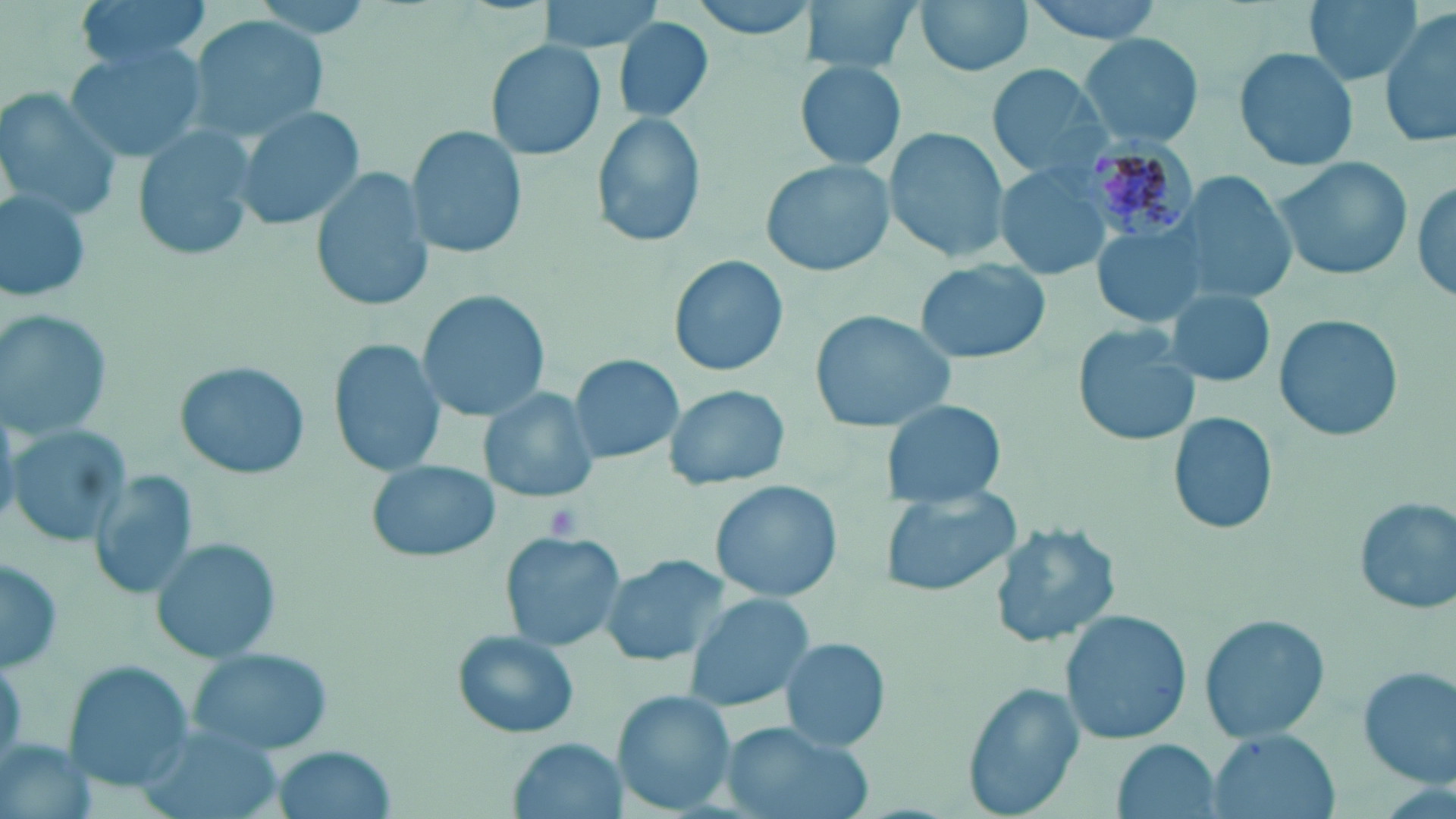 Approximate bounding boxes as [x1, y1, x2, y2] in pixels. Uninfected red blood cell locations: [73, 0, 216, 67], [533, 0, 667, 52], [683, 0, 818, 40], [806, 0, 920, 71], [913, 0, 1035, 78], [1016, 0, 1172, 43], [1304, 0, 1424, 86], [1380, 10, 1456, 147], [189, 13, 330, 138], [613, 16, 715, 122], [1077, 32, 1205, 151], [484, 38, 608, 163], [66, 45, 208, 162], [1233, 47, 1359, 172], [795, 62, 907, 170], [987, 64, 1114, 179], [1, 94, 119, 218], [232, 105, 365, 232], [588, 111, 705, 250], [134, 127, 258, 261], [408, 127, 528, 259], [883, 128, 1011, 262], [1269, 156, 1410, 283], [761, 158, 899, 276], [993, 163, 1112, 282], [313, 169, 432, 310], [1173, 169, 1298, 305], [1411, 174, 1456, 310], [0, 187, 91, 304], [1090, 221, 1209, 332], [667, 251, 791, 379], [916, 257, 1052, 366], [417, 290, 553, 425], [1165, 291, 1276, 386], [810, 308, 956, 432], [0, 310, 117, 441], [1274, 313, 1403, 443], [1074, 325, 1204, 449], [328, 339, 445, 478], [568, 354, 683, 465], [175, 361, 309, 479], [661, 383, 789, 492], [480, 387, 597, 506], [878, 398, 1009, 509], [1167, 411, 1280, 537], [6, 424, 130, 546], [366, 457, 498, 563], [90, 468, 197, 601], [710, 479, 845, 603], [878, 487, 1022, 601], [1352, 496, 1455, 616], [988, 521, 1121, 650], [499, 533, 624, 651], [153, 538, 282, 662], [599, 554, 730, 666], [0, 556, 66, 673], [685, 594, 817, 711], [1059, 606, 1191, 745], [1198, 613, 1329, 745], [449, 629, 581, 741], [780, 636, 891, 752], [187, 646, 336, 757], [61, 661, 194, 791], [1356, 665, 1456, 789], [960, 680, 1088, 818], [614, 689, 735, 812], [719, 721, 873, 819], [1206, 730, 1338, 819], [0, 735, 96, 819], [509, 736, 625, 819], [1110, 738, 1224, 819], [266, 744, 398, 819]. Plasmodium malariae-infected red blood cell locations: [1079, 129, 1199, 244]. Platelet locations: [542, 502, 586, 543]. Slide-level diagnosis: Plasmodium malariae. One field of a larger specimen. Captured at 1000x magnification. Image is 1456×819 pixels. Light microscopy. Thin blood film. May-Grünwald-Giemsa stain.